Name the cell type shown.
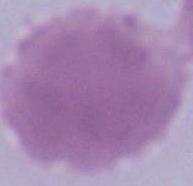
This is an erythrocyte.

modality = micrograph
magnification = 1000x